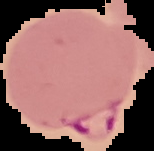

image size = 154×151 pixels
image type = segmented cell region with the area outside set to black
result = Plasmodium parasites identified
preparation = thin blood smear